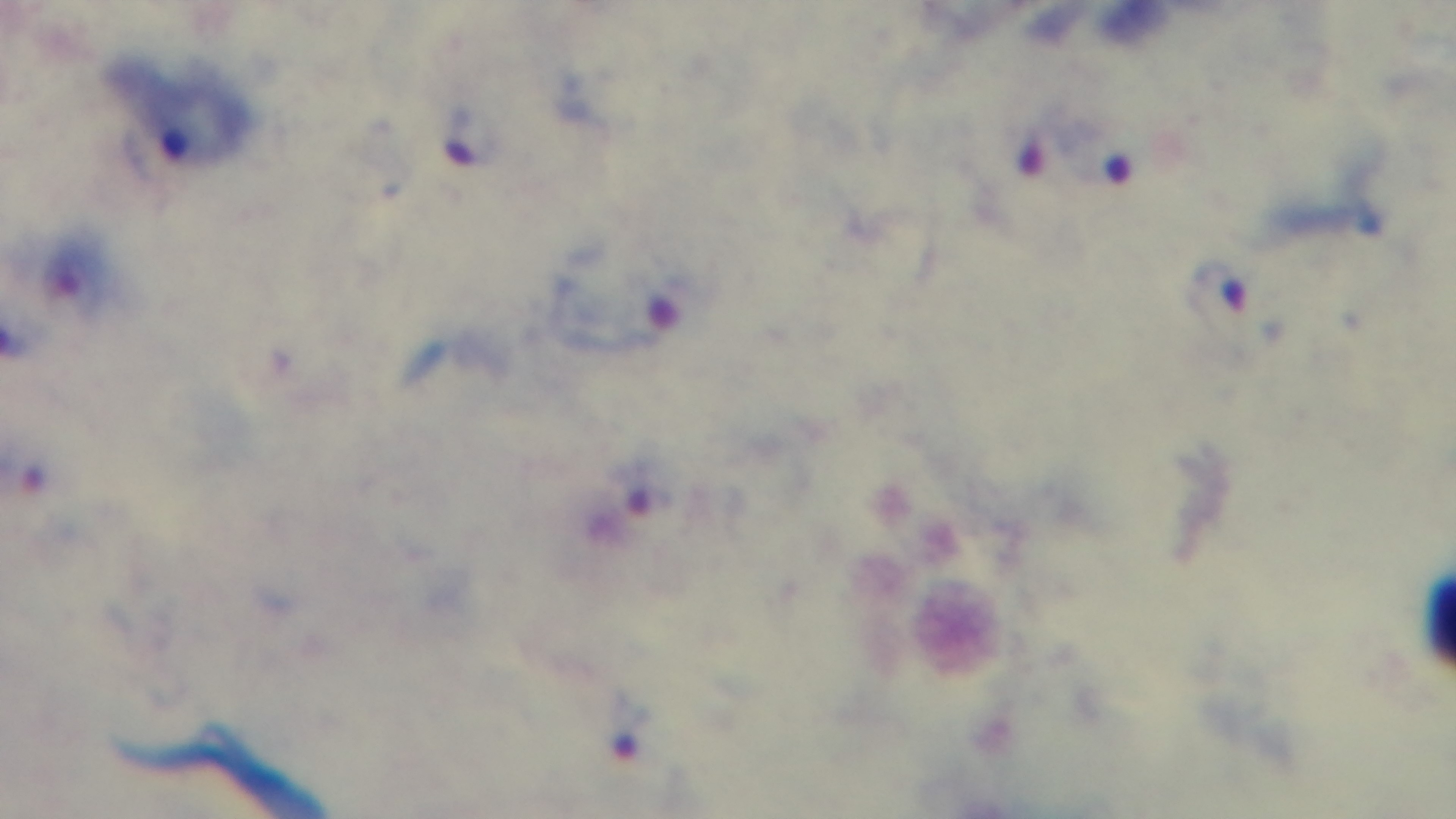
100x oil-immersion objective. Captured with a mounted 4K digital camera. Preparation: thick. Light microscopy. One field from the slide. Giemsa stain. Malaria status: positive.